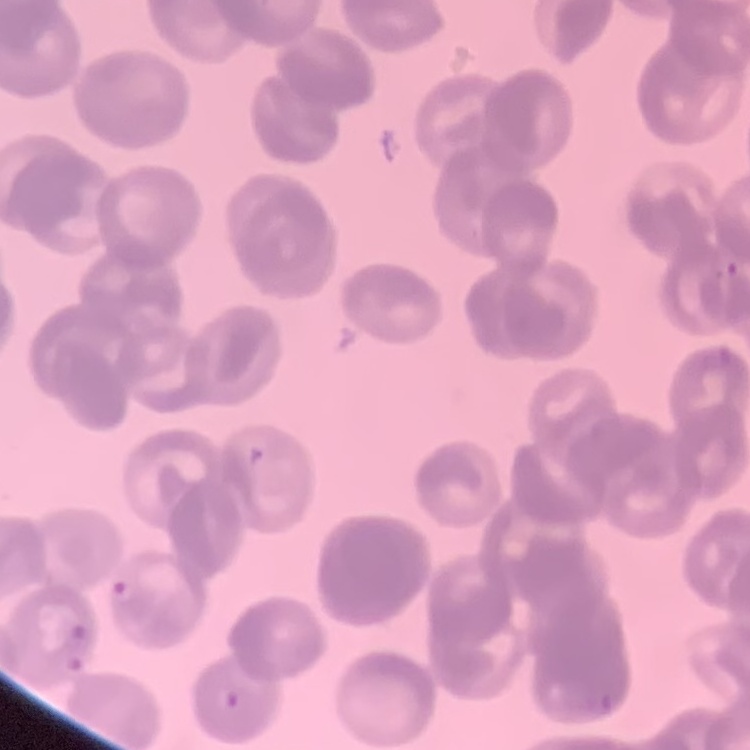

erythrocyte_morphology: rouleaux formation
stain: Field's or Giemsa
preparation: thin peripheral smear
image_type: one tile cut from a larger photomicrograph